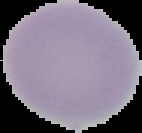

Image is 142×133 pixels. From a thin blood smear. Malaria status: uninfected. Segmented cell region on a black background.